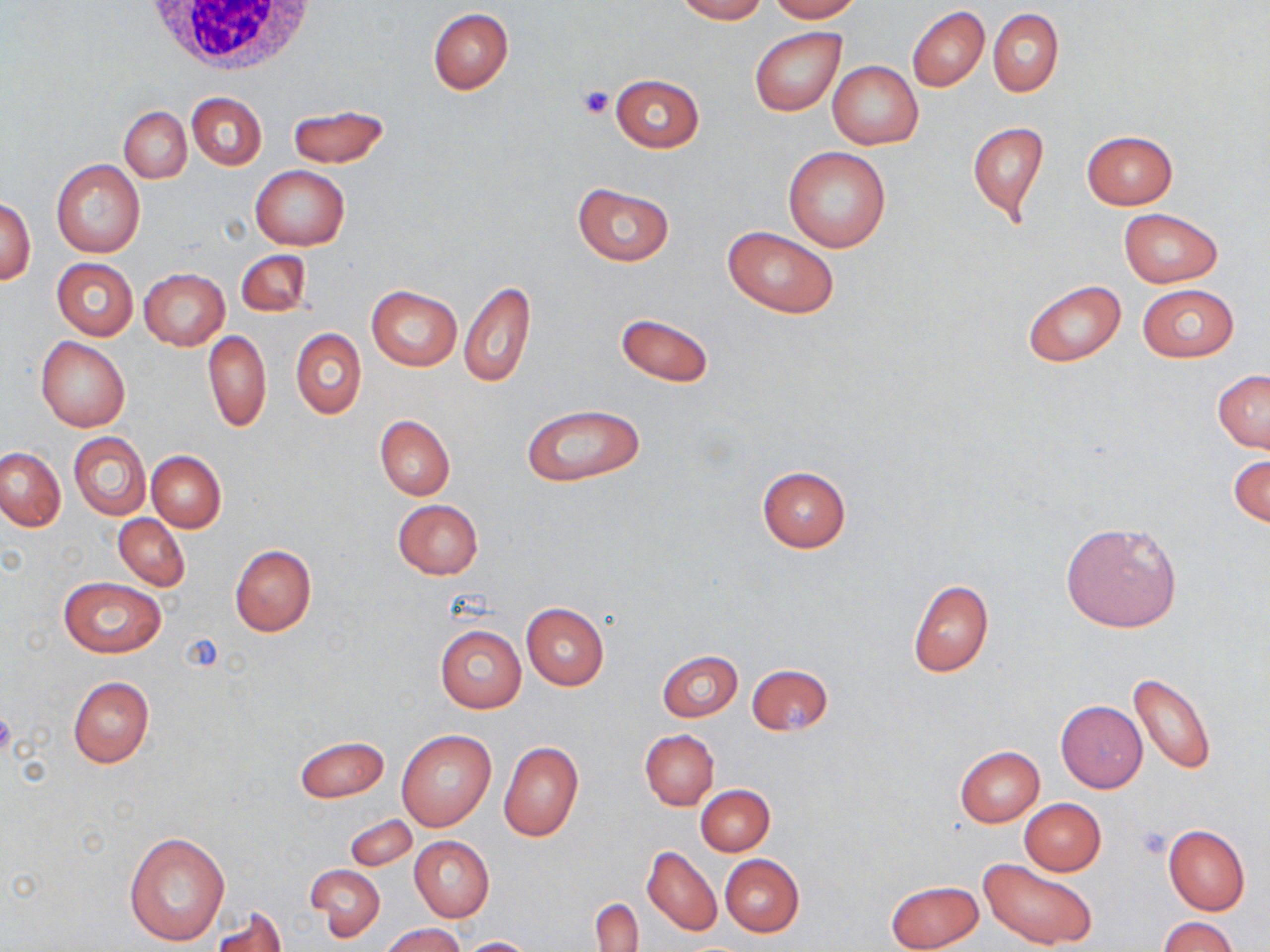
Summary:
  - Coordinate format: approximate bounding boxes as named x1/y1/x2/y2 corners in pixels
  - White blood cell locations: (x1=136, y1=1, x2=320, y2=74)
  - Uninfected red blood cell locations: (x1=674, y1=0, x2=768, y2=22), (x1=767, y1=0, x2=863, y2=22), (x1=907, y1=6, x2=989, y2=92), (x1=428, y1=8, x2=514, y2=94), (x1=989, y1=8, x2=1063, y2=95), (x1=749, y1=25, x2=846, y2=117), (x1=829, y1=60, x2=923, y2=150), (x1=609, y1=74, x2=704, y2=152), (x1=187, y1=92, x2=266, y2=171), (x1=287, y1=104, x2=391, y2=168), (x1=119, y1=108, x2=191, y2=182), (x1=966, y1=120, x2=1049, y2=223), (x1=1082, y1=130, x2=1177, y2=209), (x1=782, y1=146, x2=891, y2=253), (x1=52, y1=160, x2=144, y2=257), (x1=251, y1=165, x2=350, y2=250), (x1=572, y1=183, x2=673, y2=266), (x1=1, y1=196, x2=36, y2=285), (x1=1117, y1=207, x2=1224, y2=287), (x1=722, y1=225, x2=840, y2=319), (x1=236, y1=250, x2=311, y2=316), (x1=52, y1=258, x2=138, y2=339), (x1=140, y1=269, x2=229, y2=349), (x1=1022, y1=279, x2=1127, y2=367), (x1=459, y1=280, x2=535, y2=389), (x1=1137, y1=283, x2=1239, y2=361), (x1=367, y1=285, x2=461, y2=372), (x1=615, y1=312, x2=714, y2=388), (x1=291, y1=328, x2=366, y2=419), (x1=202, y1=330, x2=271, y2=432), (x1=36, y1=336, x2=129, y2=431), (x1=1213, y1=370, x2=1270, y2=452), (x1=520, y1=403, x2=646, y2=486), (x1=376, y1=415, x2=454, y2=500), (x1=69, y1=433, x2=150, y2=519), (x1=0, y1=447, x2=64, y2=530), (x1=147, y1=450, x2=226, y2=532), (x1=1230, y1=452, x2=1270, y2=531), (x1=757, y1=465, x2=852, y2=552), (x1=392, y1=499, x2=484, y2=579), (x1=114, y1=514, x2=190, y2=590), (x1=1060, y1=520, x2=1181, y2=633), (x1=230, y1=544, x2=315, y2=637), (x1=59, y1=576, x2=166, y2=658), (x1=907, y1=579, x2=994, y2=678), (x1=521, y1=602, x2=608, y2=690), (x1=435, y1=624, x2=526, y2=713), (x1=658, y1=652, x2=742, y2=721), (x1=747, y1=663, x2=834, y2=737), (x1=1128, y1=671, x2=1215, y2=774), (x1=67, y1=676, x2=155, y2=768), (x1=1056, y1=700, x2=1147, y2=792), (x1=639, y1=729, x2=719, y2=809), (x1=397, y1=730, x2=496, y2=831), (x1=294, y1=736, x2=389, y2=802), (x1=498, y1=741, x2=583, y2=842), (x1=954, y1=746, x2=1045, y2=827), (x1=696, y1=784, x2=774, y2=856), (x1=1019, y1=798, x2=1106, y2=875), (x1=345, y1=814, x2=417, y2=871), (x1=1162, y1=825, x2=1250, y2=914), (x1=124, y1=830, x2=230, y2=945), (x1=409, y1=836, x2=494, y2=922), (x1=642, y1=845, x2=721, y2=937), (x1=721, y1=854, x2=804, y2=937), (x1=980, y1=858, x2=1099, y2=950), (x1=308, y1=866, x2=385, y2=939), (x1=885, y1=879, x2=983, y2=952), (x1=592, y1=897, x2=643, y2=952), (x1=213, y1=907, x2=287, y2=951), (x1=1160, y1=916, x2=1238, y2=952), (x1=381, y1=923, x2=466, y2=952), (x1=457, y1=937, x2=539, y2=952)
  - Platelet locations: (x1=578, y1=86, x2=615, y2=119), (x1=0, y1=709, x2=15, y2=755), (x1=1133, y1=827, x2=1171, y2=860)
  - Slide-level diagnosis: negative for blood parasites
  - Image size: 1270×952 pixels
  - Stain: May-Grünwald-Giemsa
  - Preparation: thin blood film
  - Magnification: 1000x
  - Field of view: single
  - Modality: optical microscopy